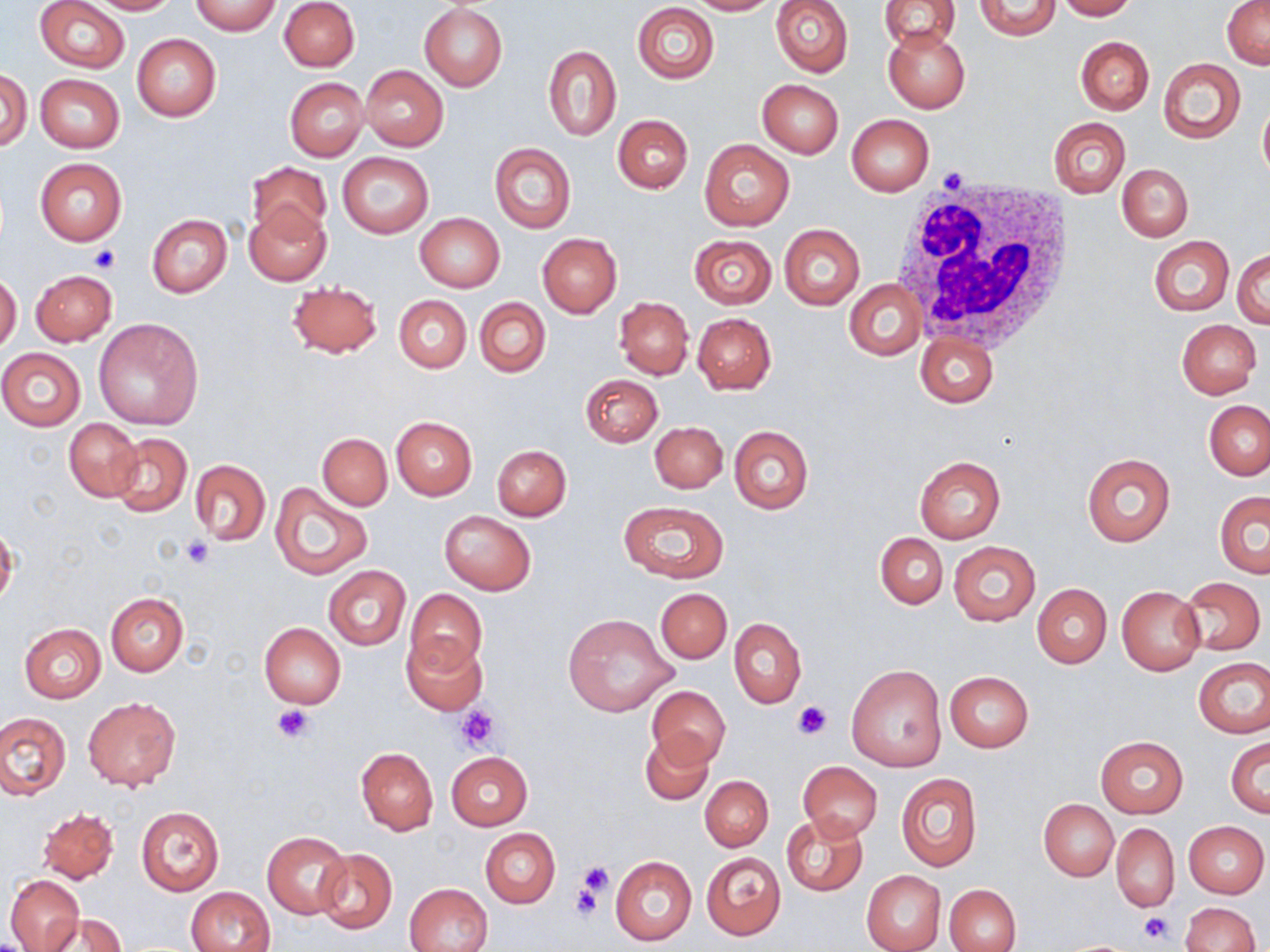

Summary:
  - Coordinate format: approximate bounding boxes as (x1,y1)-(x2,y2) corner pairs in pixels
  - Uninfected red blood cell locations: (36,0)-(129,72), (86,0)-(179,14), (280,0)-(360,72), (688,0)-(779,15), (771,0)-(853,77), (880,0)-(961,51), (975,0)-(1059,40), (1055,0)-(1138,20), (190,1)-(282,36), (1222,1)-(1270,70), (632,2)-(719,83), (420,4)-(508,90), (882,25)-(970,112), (132,33)-(221,121), (1075,36)-(1154,114), (543,46)-(621,140), (1158,58)-(1245,144), (361,66)-(448,151), (1,67)-(31,151), (35,73)-(124,152), (285,77)-(368,161), (756,79)-(843,158), (1258,99)-(1270,186), (846,114)-(934,196), (613,115)-(693,193), (1049,118)-(1130,197), (699,139)-(795,231), (489,143)-(575,233), (336,151)-(434,239), (35,158)-(127,245), (246,162)-(330,241), (1117,164)-(1193,241), (245,204)-(332,286), (415,213)-(505,292), (147,215)-(233,297), (780,224)-(865,310), (537,233)-(621,317), (689,234)-(776,309), (1148,236)-(1234,317), (1234,248)-(1270,329), (30,269)-(118,345), (0,273)-(21,355), (286,281)-(383,357), (846,282)-(925,360), (395,295)-(471,374), (615,296)-(693,379), (475,297)-(550,377), (693,313)-(776,394), (94,319)-(206,431), (1176,319)-(1262,398), (914,332)-(997,407), (0,348)-(87,430), (580,374)-(663,447), (1203,400)-(1269,479), (391,416)-(476,500), (64,418)-(143,502), (649,421)-(728,493), (728,425)-(814,514), (108,433)-(192,516), (317,433)-(392,509), (492,444)-(572,520), (1081,453)-(1176,548), (914,456)-(1006,543), (190,460)-(270,545), (271,483)-(371,580), (1214,491)-(1270,577), (616,500)-(730,582), (440,510)-(536,595), (0,524)-(18,610), (875,533)-(947,609), (948,541)-(1041,626), (323,566)-(410,650), (1181,576)-(1266,655), (1032,583)-(1112,668), (1117,586)-(1206,676), (656,588)-(732,663), (406,589)-(488,675), (106,593)-(188,675), (562,613)-(679,716), (729,618)-(806,708), (19,623)-(107,703), (259,623)-(347,708), (400,635)-(487,715), (1194,657)-(1270,738), (846,664)-(947,772), (944,670)-(1033,753), (646,686)-(731,769), (83,694)-(180,791), (0,712)-(70,799), (638,731)-(714,805), (1097,736)-(1188,817), (1227,738)-(1269,817), (356,747)-(438,835), (446,751)-(532,829), (798,760)-(882,841), (896,772)-(982,871), (700,775)-(773,851), (1039,800)-(1118,880), (135,806)-(224,896), (37,808)-(119,883), (782,813)-(869,897), (1184,821)-(1268,897), (1111,824)-(1178,912), (480,828)-(560,908), (261,831)-(350,919), (314,848)-(397,933), (701,852)-(786,939), (611,855)-(696,945), (860,870)-(947,952), (5,873)-(84,951), (944,883)-(1021,952), (405,884)-(491,951), (185,887)-(275,951), (1179,902)-(1259,952), (41,913)-(126,952)
  - White blood cell locations: (892,177)-(1078,354)
  - Platelet locations: (935,166)-(971,192), (91,245)-(121,272), (179,535)-(214,569), (793,701)-(831,740), (456,704)-(498,750), (274,705)-(316,744), (575,860)-(614,902), (570,879)-(606,924), (1137,911)-(1174,945)
  - Slide-level diagnosis: no evidence of blood parasites
  - Magnification: 1000x
  - Field of view: single
  - Modality: light microscopy
  - Stain: May-Grünwald-Giemsa
  - Preparation: thin blood film
  - Image size: 1270×952 pixels